Classify this cell by malaria status.
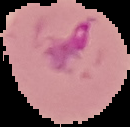
Parasitized.

Summary:
  - Preparation: thin blood smear
  - Image size: 130×127 pixels
  - Image type: segmented cell region on a black background